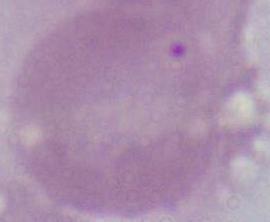 Photomicrograph. 1000x magnification. A red blood cell is seen.